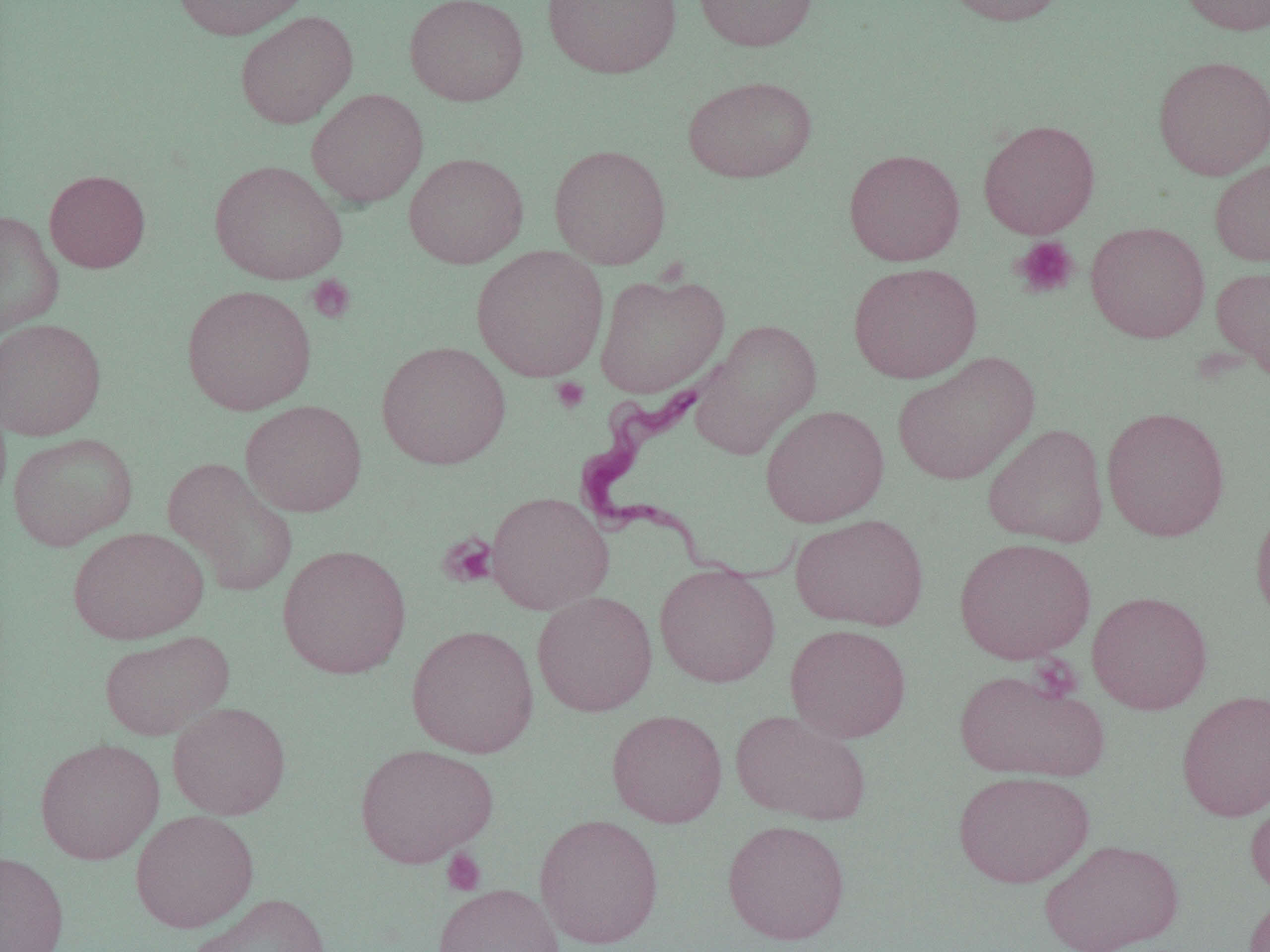

Approximate bounding boxes as named x1/y1/x2/y2 corners in pixels. Uninfected red blood cell locations: (x1=171, y1=0, x2=310, y2=40), (x1=404, y1=0, x2=528, y2=106), (x1=542, y1=0, x2=682, y2=79), (x1=693, y1=0, x2=819, y2=52), (x1=940, y1=0, x2=1072, y2=26), (x1=1178, y1=0, x2=1270, y2=36), (x1=235, y1=10, x2=358, y2=129), (x1=1153, y1=55, x2=1270, y2=179), (x1=682, y1=75, x2=817, y2=183), (x1=307, y1=89, x2=428, y2=208), (x1=978, y1=119, x2=1100, y2=239), (x1=549, y1=144, x2=671, y2=269), (x1=843, y1=148, x2=965, y2=266), (x1=403, y1=153, x2=529, y2=269), (x1=1209, y1=157, x2=1270, y2=267), (x1=209, y1=160, x2=347, y2=285), (x1=44, y1=170, x2=150, y2=273), (x1=0, y1=210, x2=64, y2=337), (x1=1085, y1=221, x2=1210, y2=342), (x1=471, y1=245, x2=609, y2=381), (x1=848, y1=262, x2=982, y2=383), (x1=1211, y1=265, x2=1270, y2=378), (x1=593, y1=271, x2=729, y2=398), (x1=181, y1=284, x2=317, y2=415), (x1=0, y1=318, x2=106, y2=440), (x1=691, y1=320, x2=822, y2=459), (x1=376, y1=341, x2=511, y2=469), (x1=891, y1=350, x2=1039, y2=485), (x1=241, y1=400, x2=367, y2=517), (x1=760, y1=404, x2=889, y2=527), (x1=1101, y1=406, x2=1231, y2=542), (x1=983, y1=423, x2=1108, y2=546), (x1=7, y1=432, x2=138, y2=550), (x1=163, y1=457, x2=298, y2=596), (x1=487, y1=491, x2=614, y2=614), (x1=1251, y1=500, x2=1270, y2=629), (x1=790, y1=513, x2=929, y2=632), (x1=67, y1=526, x2=209, y2=644), (x1=954, y1=537, x2=1096, y2=664), (x1=277, y1=544, x2=412, y2=679), (x1=654, y1=563, x2=781, y2=687), (x1=532, y1=590, x2=657, y2=717), (x1=1087, y1=590, x2=1213, y2=715), (x1=406, y1=624, x2=539, y2=758), (x1=785, y1=624, x2=911, y2=743), (x1=99, y1=630, x2=233, y2=740), (x1=954, y1=668, x2=1110, y2=783), (x1=1176, y1=689, x2=1270, y2=822), (x1=167, y1=702, x2=291, y2=820), (x1=730, y1=708, x2=872, y2=825), (x1=606, y1=709, x2=728, y2=827), (x1=35, y1=737, x2=165, y2=864), (x1=354, y1=742, x2=499, y2=868), (x1=953, y1=770, x2=1094, y2=888), (x1=1245, y1=789, x2=1270, y2=898), (x1=129, y1=809, x2=259, y2=932), (x1=534, y1=813, x2=664, y2=949), (x1=722, y1=819, x2=850, y2=945), (x1=1039, y1=838, x2=1185, y2=952), (x1=0, y1=851, x2=70, y2=952), (x1=432, y1=883, x2=564, y2=952), (x1=1243, y1=891, x2=1270, y2=952), (x1=187, y1=892, x2=332, y2=952). Trypanosoma brucei locations: (x1=576, y1=384, x2=803, y2=587). Platelet locations: (x1=1012, y1=236, x2=1079, y2=299), (x1=307, y1=275, x2=356, y2=323), (x1=550, y1=377, x2=590, y2=413), (x1=438, y1=533, x2=498, y2=588), (x1=441, y1=848, x2=486, y2=895). Slide-level diagnosis: Trypanosoma brucei. Image is 1270×952 pixels. Thin blood film. Light microscopy. Single field of view. 1000x magnification.